Report the malaria status of this cell.
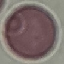

Uninfected.

Automatically extracted cell patch, resized to 64 × 64 pixels. Acquired by smartphone through the microscope eyepiece. Thin blood film. Giemsa-stained preparation.